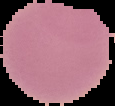

Summary:
  - Image type: cell region segmented out of the field of view; surrounding area masked to black
  - Result: negative for malaria parasites
  - Preparation: thin blood smear
  - Image size: 115×106 pixels